Comment on the morphology of the erythrocytes.
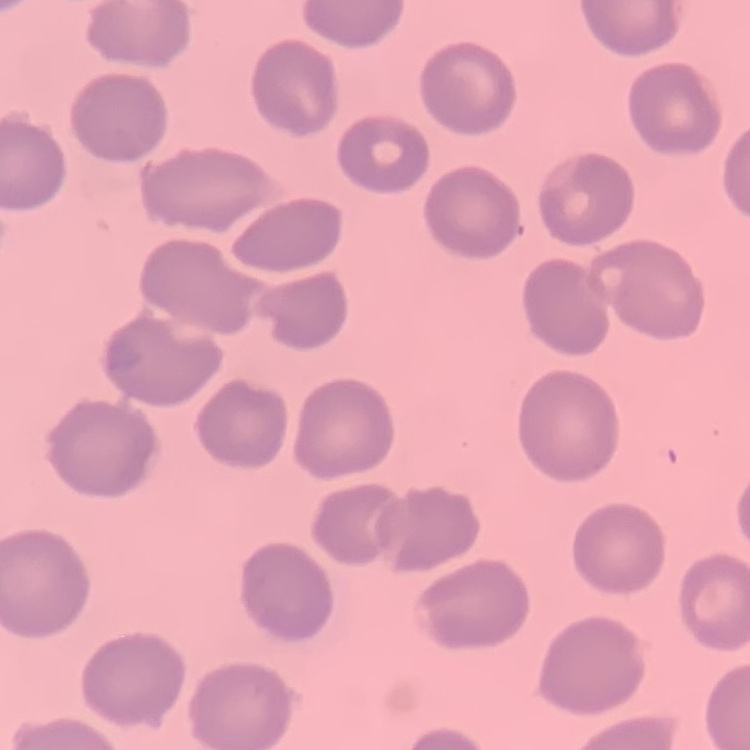

They show no rouleaux formation.

{
  "image_type": "one tile cut from a larger photomicrograph",
  "stain": "Field's or Giemsa",
  "preparation": "thin blood film"
}